Report the malaria status of this cell.
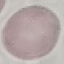

Uninfected.

Summary:
  - Preparation: thin blood film
  - Image type: automatically extracted cell patch, resized to 64 × 64 pixels
  - Capture: smartphone camera at the microscope eyepiece
  - Stain: Giemsa